Assess the morphology of the red blood cells.
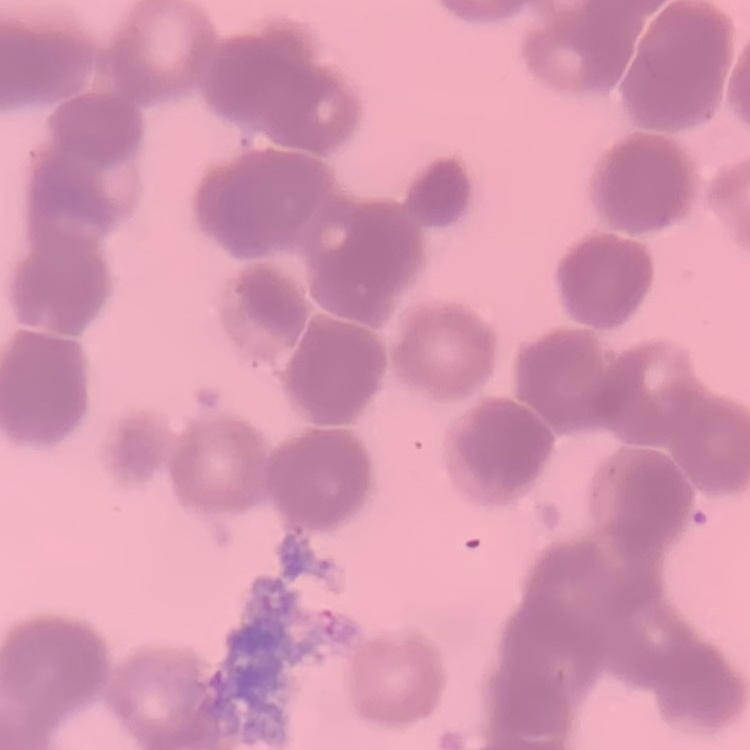

They show rouleaux formation.

{
  "image_type": "one tile cut from a larger photomicrograph",
  "preparation": "thin blood film",
  "stain": "Field's or Giemsa"
}